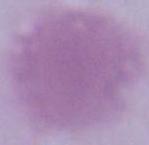
modality = micrograph
identification = red blood cell
magnification = 1000x